Locate and identify every blood parasite.
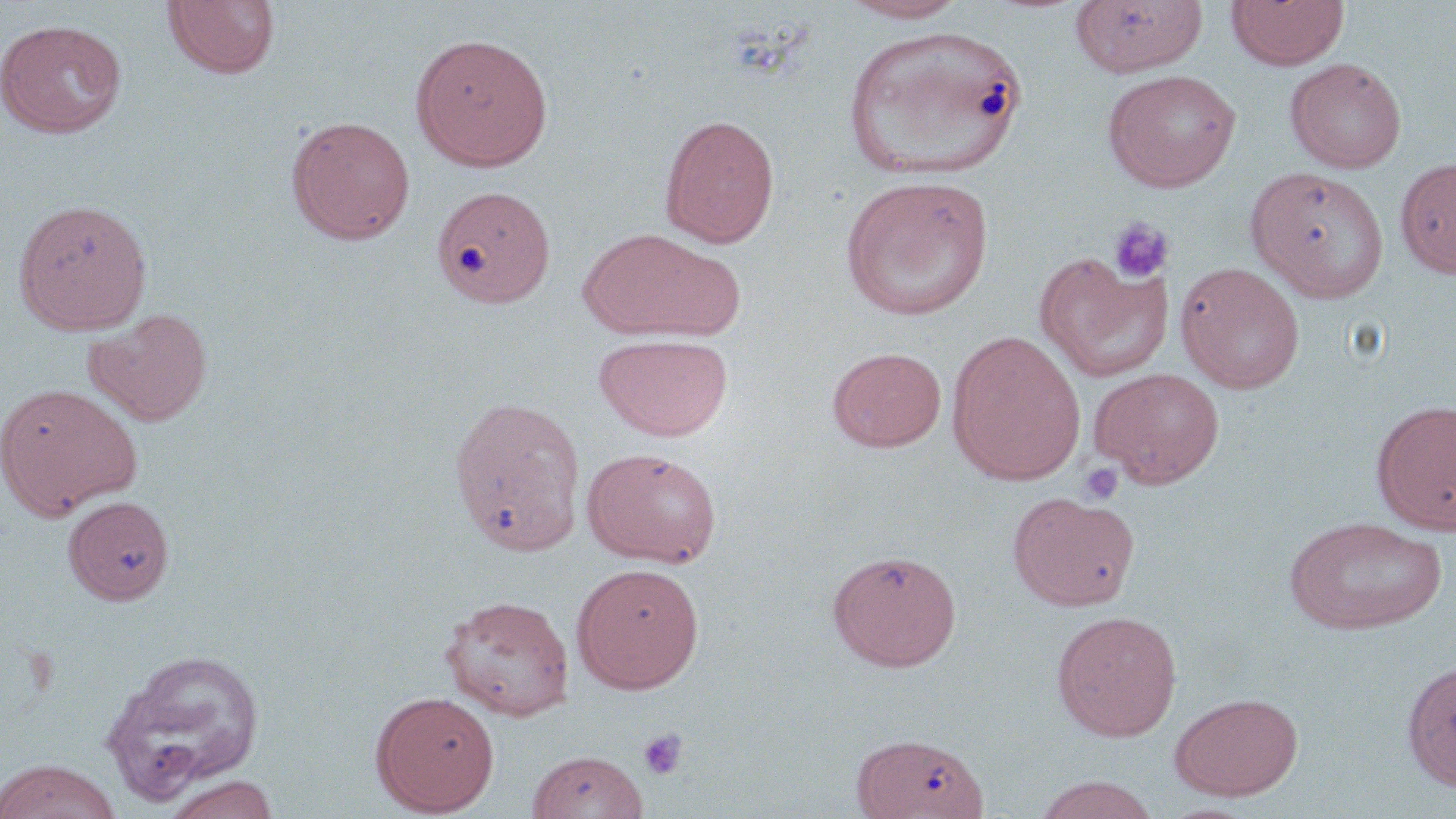
No blood parasites seen.

Summary:
  - Coordinate format: approximate bounding boxes as (x1, y1, x2, y2) in pixels
  - Uninfected red blood cell locations: (838, 0, 971, 24), (1071, 0, 1209, 76), (1226, 0, 1349, 70), (163, 1, 281, 80), (0, 19, 127, 139), (842, 25, 1028, 182), (410, 32, 553, 171), (1285, 58, 1406, 173), (1102, 69, 1241, 192), (659, 113, 781, 247), (286, 114, 416, 245), (1395, 157, 1456, 278), (1246, 167, 1389, 302), (840, 174, 995, 321), (432, 185, 555, 309), (12, 198, 153, 334), (578, 227, 739, 341), (1034, 253, 1173, 382), (1175, 261, 1306, 393), (85, 308, 212, 427), (947, 330, 1086, 484), (594, 333, 734, 441), (827, 346, 947, 452), (1090, 367, 1225, 487), (1, 382, 142, 519), (448, 395, 587, 556), (1371, 398, 1456, 534), (583, 447, 722, 568), (1008, 492, 1139, 609), (63, 496, 175, 605), (1283, 516, 1447, 635), (828, 549, 962, 671), (571, 562, 705, 693), (439, 594, 575, 721), (1050, 609, 1182, 741), (99, 648, 266, 803), (1401, 657, 1456, 791), (371, 691, 500, 816), (1169, 692, 1304, 800), (851, 732, 990, 819), (526, 749, 649, 818), (0, 759, 122, 819), (161, 774, 280, 819), (1033, 774, 1161, 819)
  - Platelet locations: (1107, 217, 1173, 284), (1077, 462, 1125, 505), (638, 729, 688, 780)
  - Slide-level diagnosis: negative for blood parasites
  - Preparation: thin blood film
  - Modality: light microscopy
  - Field of view: single
  - Image size: 1456×819 pixels
  - Stain: May-Grünwald-Giemsa
  - Magnification: 1000x